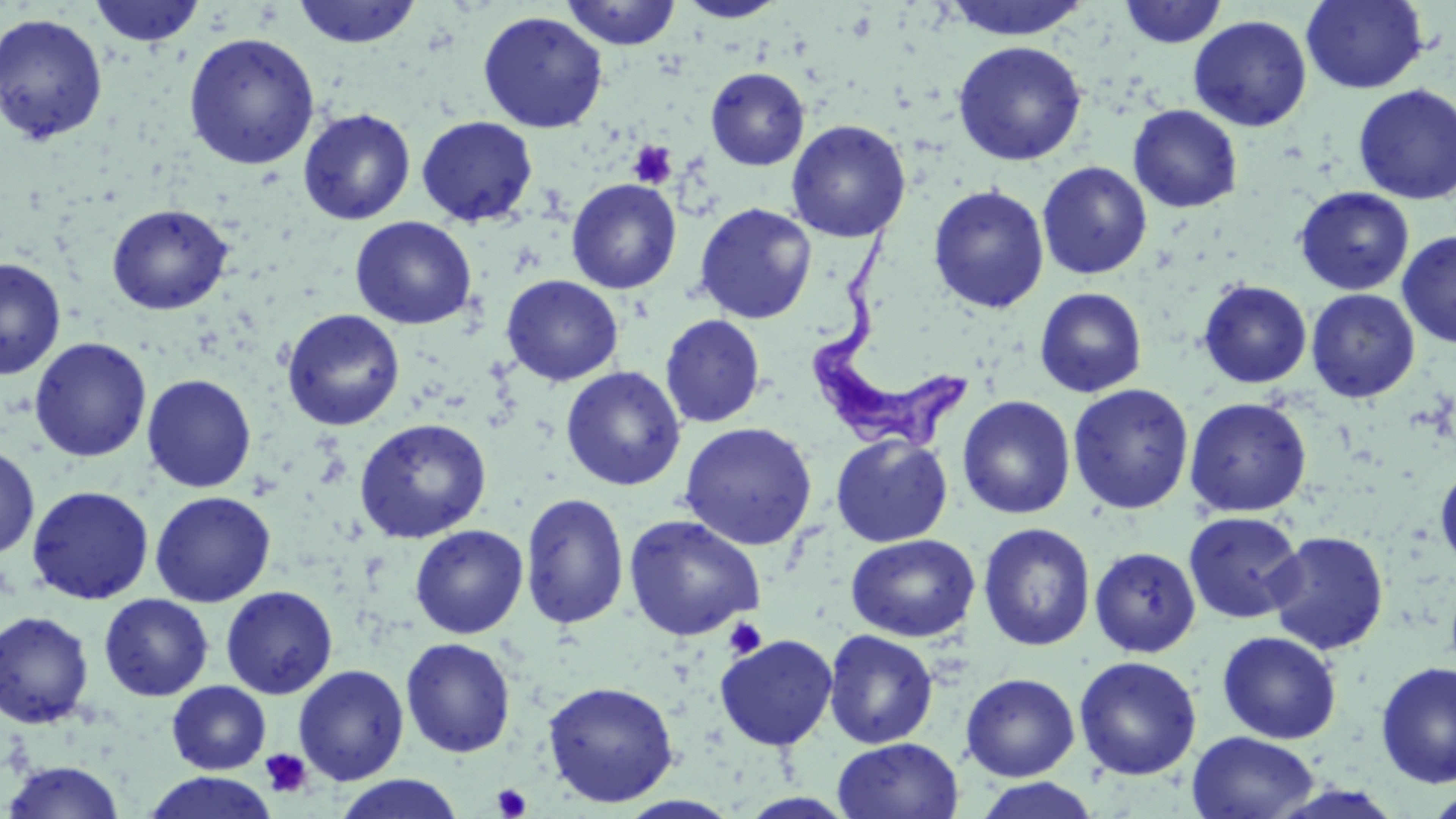

{
  "trypanosoma_brucei_locations": "approximate bounding boxes as (x1,y1)-(x2,y2) corner pairs in pixels: (809,217)-(970,451)",
  "slide_level_diagnosis": "Trypanosoma brucei",
  "magnification": "1000x",
  "platelet_locations": "approximate bounding boxes as (x1,y1)-(x2,y2) corner pairs in pixels: (628,141)-(677,189), (722,617)-(767,660), (259,748)-(312,798), (492,784)-(533,818)",
  "stain": "May-Grünwald-Giemsa",
  "image_size": "1456×819 pixels",
  "preparation": "thin blood smear",
  "modality": "optical microscopy",
  "field_of_view": "single",
  "uninfected_red_blood_cell_locations": "approximate bounding boxes as (x1,y1)-(x2,y2) corner pairs in pixels: (89,0)-(206,48), (292,0)-(422,49), (561,0)-(681,50), (676,0)-(788,22), (940,0)-(1091,41), (1301,0)-(1428,95), (1119,1)-(1227,48), (477,11)-(608,133), (0,13)-(108,145), (1188,15)-(1312,132), (183,33)-(320,170), (952,40)-(1087,166), (705,67)-(810,171), (1353,84)-(1456,205), (1128,104)-(1243,213), (298,109)-(416,225), (416,116)-(538,227), (786,119)-(911,242), (1037,161)-(1153,279), (566,178)-(682,294), (928,185)-(1050,314), (1293,187)-(1414,295), (694,202)-(817,324), (107,203)-(233,315), (350,216)-(477,329), (1397,229)-(1456,348), (0,258)-(66,379), (501,274)-(624,386), (1198,280)-(1312,389), (1034,288)-(1148,398), (1305,288)-(1420,403), (281,309)-(405,431), (660,314)-(766,428), (29,337)-(151,463), (560,366)-(686,491), (141,374)-(256,493), (1067,383)-(1194,515), (957,395)-(1075,519), (1184,397)-(1312,517), (353,417)-(491,543), (679,422)-(817,550), (830,433)-(953,548), (0,444)-(40,560), (1434,463)-(1456,574), (26,485)-(154,605), (150,491)-(276,607), (520,492)-(630,630), (1183,511)-(1305,624), (624,514)-(765,641), (977,522)-(1096,652), (410,525)-(528,638), (1265,531)-(1389,654), (845,533)-(980,642), (1090,547)-(1201,657), (220,585)-(338,699), (98,593)-(214,702), (0,610)-(94,729), (822,629)-(939,749), (1216,631)-(1342,744), (714,634)-(838,750), (400,637)-(517,758), (1074,656)-(1202,780), (1375,660)-(1456,789), (293,665)-(409,786), (960,673)-(1080,781), (542,680)-(679,808), (167,681)-(271,774), (1187,731)-(1320,819), (833,737)-(963,819), (3,760)-(126,818), (142,771)-(278,818), (333,774)-(464,819), (972,777)-(1100,819), (1425,789)-(1456,818)"
}